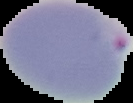
{
  "image_type": "segmented cell region on a black background",
  "preparation": "thin blood smear",
  "malaria_status": "parasitized",
  "image_size": "133×103 pixels"
}